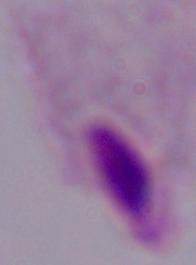 Micrograph. A trichomonad is shown. 1000x magnification.